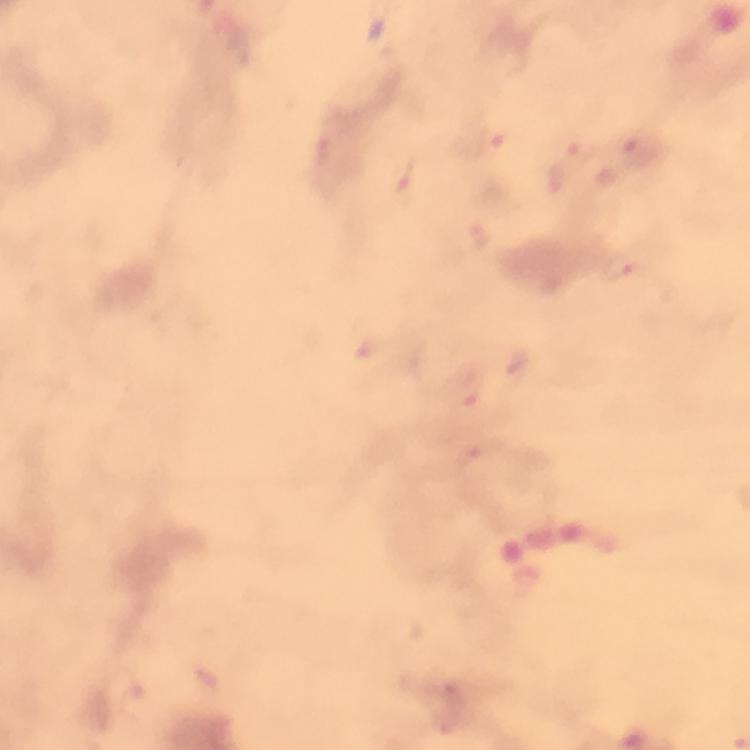

Approximate object centers, in pixels from the top-left corner. Malaria parasite locations: (x=500, y=144), (x=406, y=183), (x=621, y=267), (x=470, y=391). Immersion oil applied. Image is 750×750 pixels. Smartphone photograph taken through a microscope. At 100x magnification. From a malaria diagnostic workup. Giemsa stain. Cropped region of a single field of view. Thick blood film.